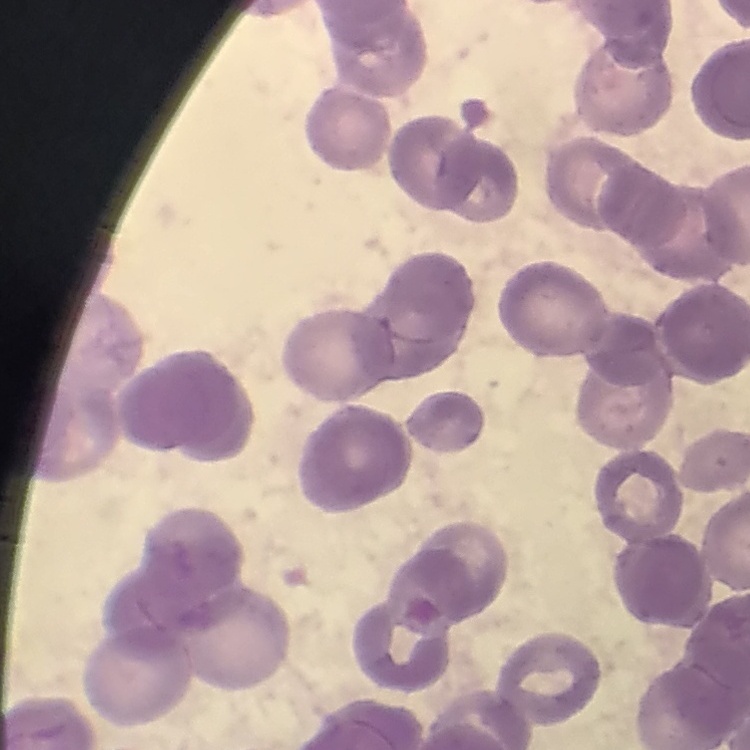

Summary:
  - Erythrocyte morphology: rouleaux formation
  - Preparation: thin blood film
  - Stain: Field's or Giemsa
  - Image type: square crop of a larger photomicrograph